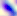
magnification = 400x
identification = Toxoplasma gondii
modality = photomicrograph